Report the malaria status of this cell.
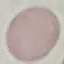
Uninfected.

capture = smartphone camera at the microscope eyepiece
stain = Giemsa
preparation = thin smear
image type = cell patch, automatically extracted from a larger field of view and resized to 64 × 64 pixels